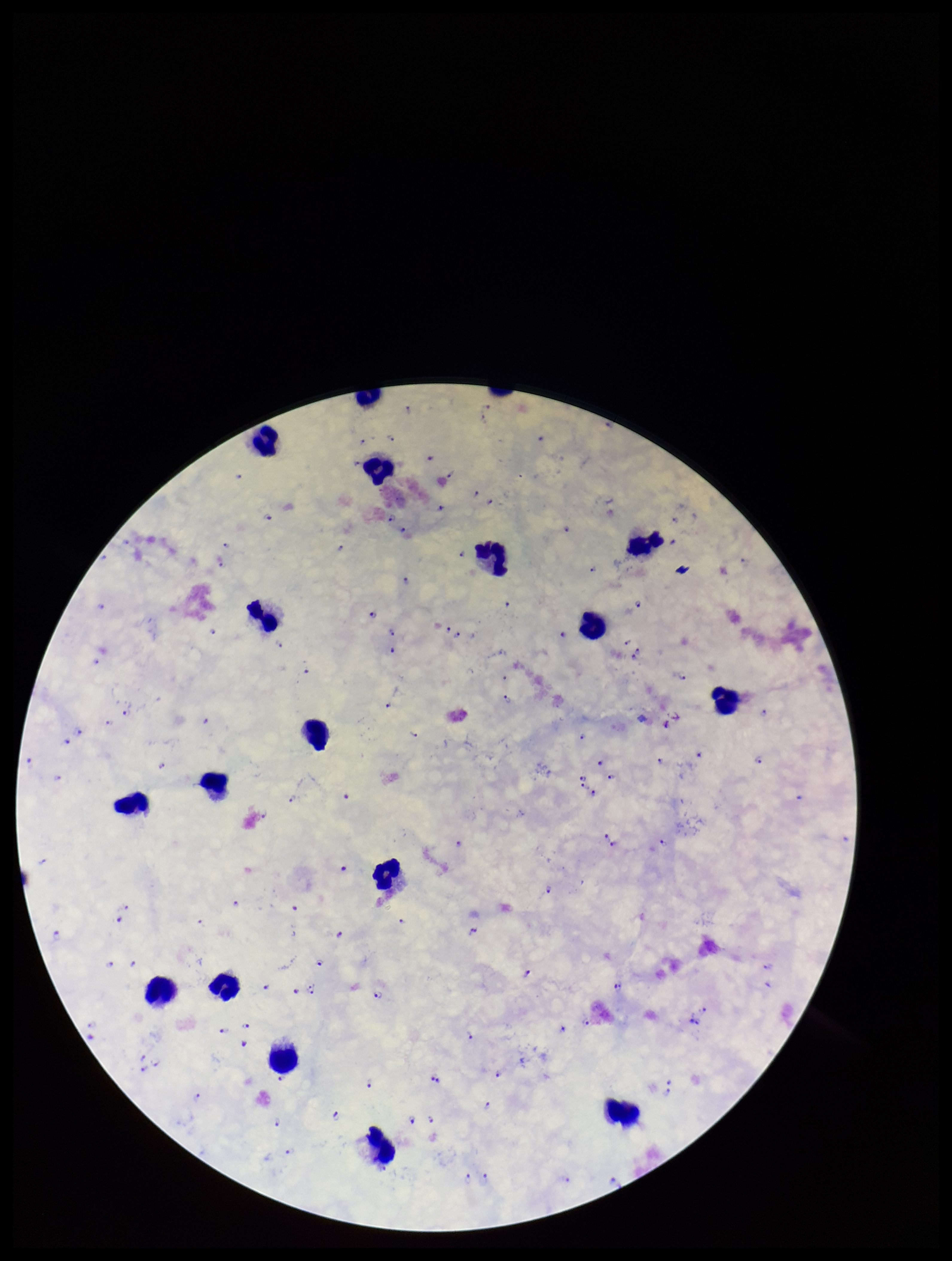

leukocyte count = 18
capture = smartphone photograph through the microscope eyepiece
image size = 952×1261 pixels
parasite count = 120
Plasmodium parasites = detected
preparation = thick smear
field of view = one from this slide
species reported for this patient = Plasmodium falciparum
stain = Giemsa
patient malaria status = infected